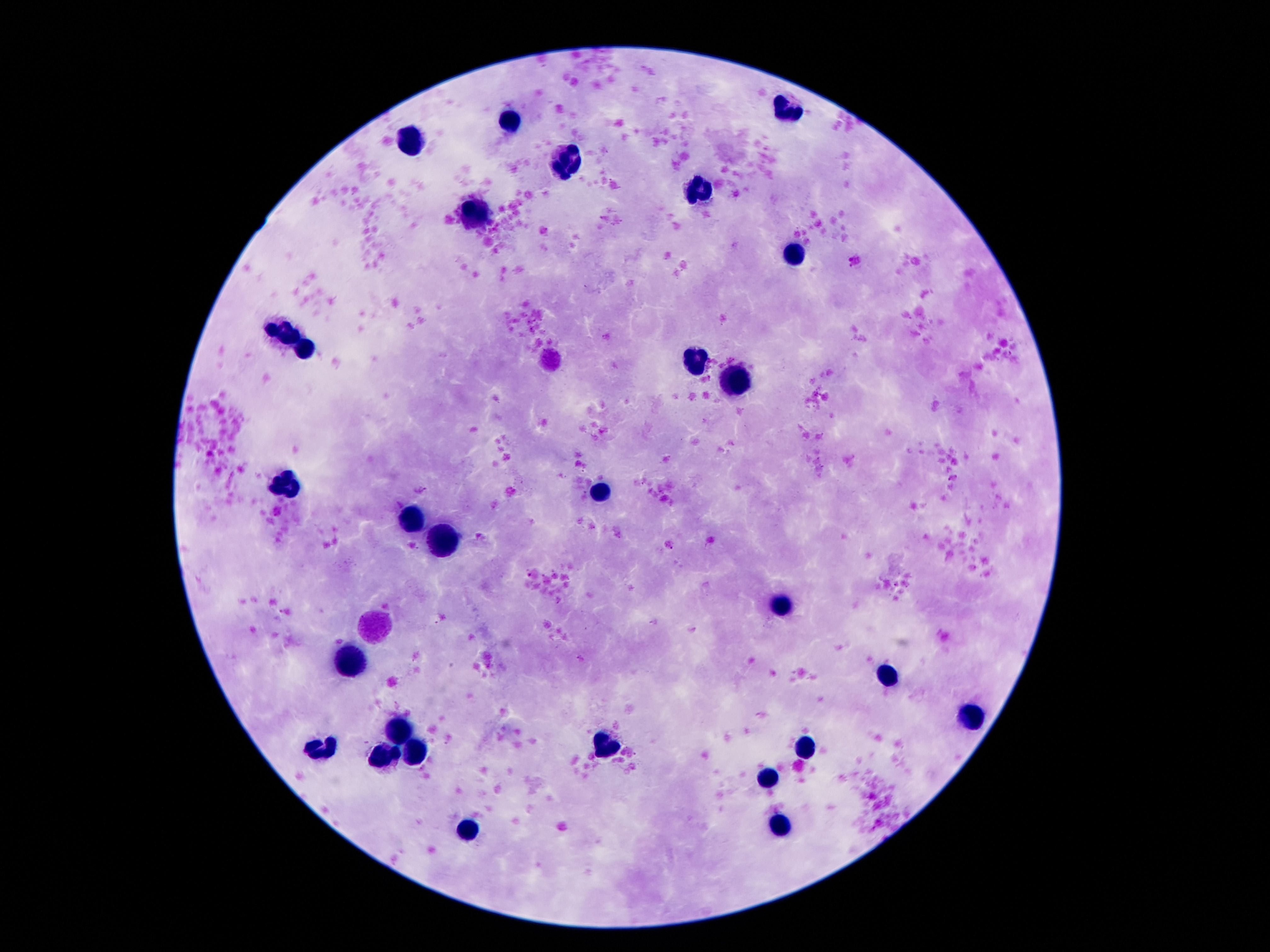

leukocyte locations = approximate centers as (x, y) in pixels: (790, 108), (507, 122), (412, 145), (567, 161), (702, 192), (474, 214), (793, 256), (284, 329), (306, 347), (698, 355), (731, 385), (284, 484), (598, 493), (403, 522), (441, 542), (784, 604), (348, 661), (888, 677), (972, 717), (401, 733), (808, 744), (605, 745), (417, 748), (317, 750), (388, 752), (768, 777), (782, 825), (470, 830)
capture = smartphone camera through the microscope eyepiece
image size = 1270×952 pixels
patient malaria status = negative
preparation = thick blood smear
stain = Giemsa
field of view = one from this slide
magnification = 100x